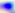
Summary:
  - Magnification: 400x
  - Modality: micrograph
  - Identification: Toxoplasma gondii